Locate every Plasmodium vivax-infected red blood cell.
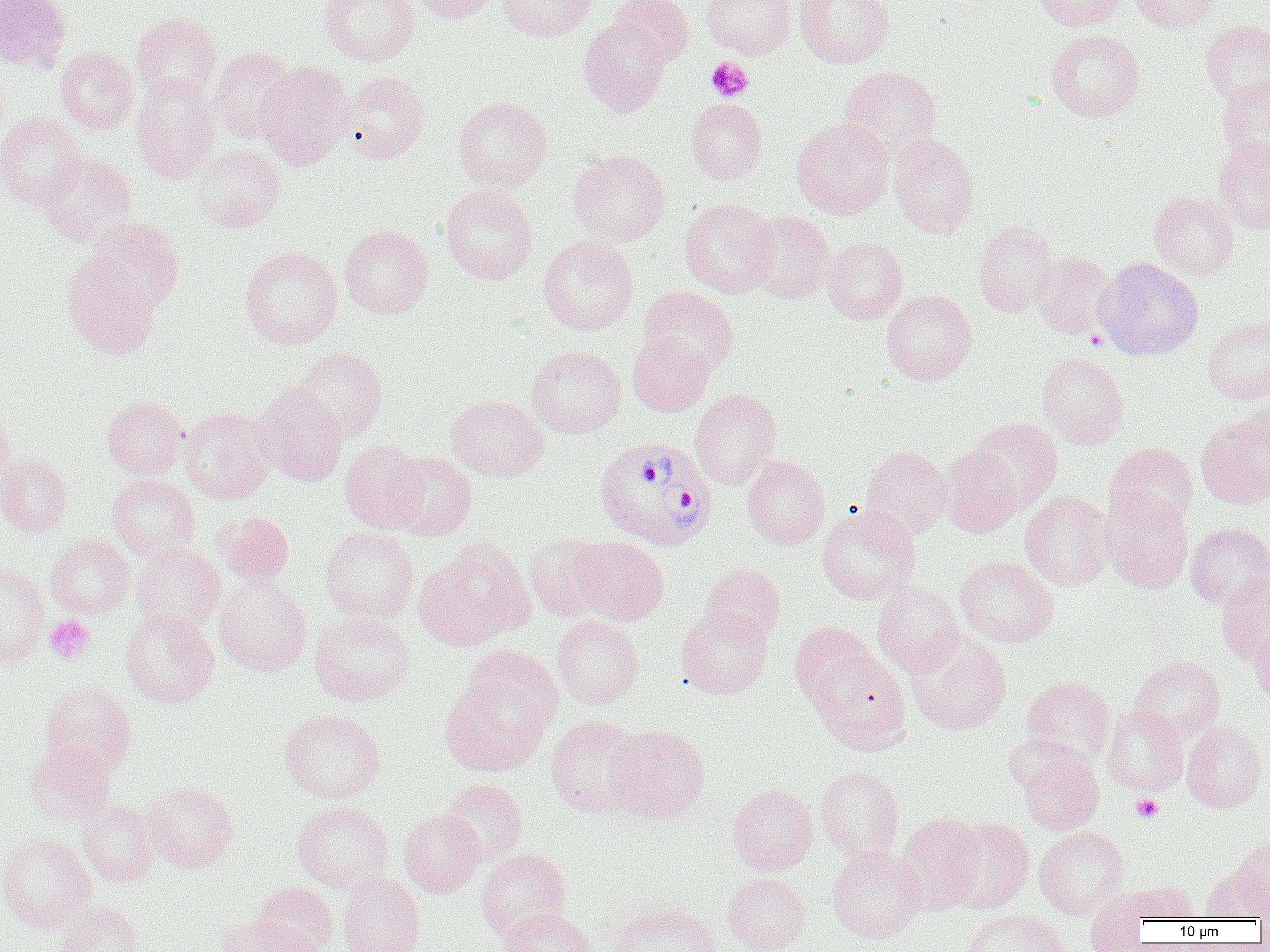
Approximate bounding boxes as named x1/y1/x2/y2 corners in pixels.
Plasmodium vivax-infected red blood cells: (x1=593, y1=436, x2=718, y2=552).

Summary:
  - Uninfected red blood cell locations: (x1=0, y1=0, x2=70, y2=73), (x1=320, y1=0, x2=419, y2=66), (x1=411, y1=0, x2=501, y2=23), (x1=497, y1=0, x2=596, y2=41), (x1=611, y1=0, x2=694, y2=66), (x1=702, y1=0, x2=795, y2=58), (x1=794, y1=0, x2=895, y2=68), (x1=1031, y1=0, x2=1128, y2=31), (x1=1130, y1=0, x2=1219, y2=33), (x1=131, y1=13, x2=222, y2=103), (x1=579, y1=17, x2=670, y2=116), (x1=1201, y1=20, x2=1270, y2=107), (x1=1046, y1=29, x2=1144, y2=121), (x1=55, y1=46, x2=137, y2=133), (x1=210, y1=47, x2=298, y2=142), (x1=254, y1=60, x2=353, y2=169), (x1=839, y1=65, x2=941, y2=157), (x1=340, y1=72, x2=430, y2=164), (x1=132, y1=75, x2=221, y2=183), (x1=1216, y1=76, x2=1270, y2=163), (x1=453, y1=96, x2=552, y2=191), (x1=686, y1=98, x2=767, y2=183), (x1=0, y1=113, x2=86, y2=209), (x1=791, y1=118, x2=894, y2=219), (x1=889, y1=132, x2=979, y2=237), (x1=1214, y1=136, x2=1270, y2=233), (x1=191, y1=144, x2=286, y2=232), (x1=568, y1=149, x2=671, y2=245), (x1=37, y1=152, x2=137, y2=245), (x1=440, y1=185, x2=538, y2=284), (x1=1149, y1=191, x2=1239, y2=280), (x1=679, y1=198, x2=779, y2=297), (x1=746, y1=211, x2=834, y2=304), (x1=87, y1=217, x2=185, y2=311), (x1=973, y1=220, x2=1058, y2=316), (x1=339, y1=225, x2=434, y2=318), (x1=538, y1=235, x2=638, y2=334), (x1=822, y1=235, x2=908, y2=324), (x1=240, y1=246, x2=343, y2=349), (x1=1031, y1=251, x2=1116, y2=338), (x1=63, y1=254, x2=160, y2=359), (x1=1094, y1=257, x2=1204, y2=360), (x1=639, y1=286, x2=739, y2=376), (x1=881, y1=290, x2=978, y2=385), (x1=1203, y1=316, x2=1270, y2=404), (x1=627, y1=331, x2=713, y2=415), (x1=526, y1=345, x2=626, y2=438), (x1=291, y1=347, x2=388, y2=442), (x1=1037, y1=352, x2=1129, y2=447), (x1=253, y1=381, x2=348, y2=486), (x1=690, y1=388, x2=782, y2=490), (x1=447, y1=395, x2=548, y2=480), (x1=101, y1=396, x2=186, y2=478), (x1=1237, y1=400, x2=1270, y2=482), (x1=180, y1=407, x2=276, y2=503), (x1=0, y1=410, x2=16, y2=496), (x1=1195, y1=413, x2=1270, y2=509), (x1=969, y1=417, x2=1062, y2=512), (x1=339, y1=440, x2=429, y2=533), (x1=1105, y1=442, x2=1198, y2=530), (x1=860, y1=445, x2=953, y2=539), (x1=940, y1=445, x2=1024, y2=537), (x1=389, y1=452, x2=477, y2=541), (x1=0, y1=455, x2=72, y2=536), (x1=742, y1=455, x2=829, y2=550), (x1=107, y1=475, x2=200, y2=559), (x1=1020, y1=490, x2=1113, y2=590), (x1=1100, y1=490, x2=1193, y2=593), (x1=817, y1=504, x2=919, y2=605), (x1=218, y1=511, x2=294, y2=587), (x1=1185, y1=522, x2=1270, y2=609), (x1=320, y1=527, x2=419, y2=623), (x1=524, y1=534, x2=610, y2=622), (x1=45, y1=535, x2=134, y2=617), (x1=569, y1=537, x2=669, y2=625), (x1=415, y1=541, x2=534, y2=649), (x1=131, y1=544, x2=225, y2=632), (x1=954, y1=555, x2=1059, y2=647), (x1=0, y1=562, x2=49, y2=667), (x1=701, y1=562, x2=786, y2=644), (x1=1215, y1=574, x2=1270, y2=665), (x1=214, y1=577, x2=312, y2=676), (x1=871, y1=580, x2=964, y2=676), (x1=675, y1=605, x2=773, y2=699), (x1=120, y1=608, x2=219, y2=707), (x1=309, y1=612, x2=415, y2=705), (x1=552, y1=615, x2=644, y2=708), (x1=1249, y1=621, x2=1270, y2=707), (x1=790, y1=622, x2=878, y2=712), (x1=907, y1=632, x2=1011, y2=735), (x1=811, y1=650, x2=910, y2=748), (x1=1129, y1=656, x2=1226, y2=740), (x1=441, y1=670, x2=553, y2=776), (x1=1021, y1=675, x2=1115, y2=763), (x1=42, y1=682, x2=137, y2=774), (x1=1102, y1=705, x2=1188, y2=795), (x1=279, y1=709, x2=385, y2=802), (x1=546, y1=715, x2=645, y2=817), (x1=1181, y1=721, x2=1267, y2=811), (x1=604, y1=724, x2=710, y2=823), (x1=25, y1=740, x2=116, y2=823), (x1=1018, y1=749, x2=1104, y2=834), (x1=816, y1=765, x2=904, y2=861), (x1=441, y1=778, x2=528, y2=865), (x1=143, y1=781, x2=238, y2=872), (x1=728, y1=783, x2=818, y2=874), (x1=77, y1=799, x2=159, y2=886), (x1=292, y1=801, x2=394, y2=892), (x1=399, y1=808, x2=485, y2=897), (x1=895, y1=812, x2=986, y2=913), (x1=944, y1=817, x2=1034, y2=913), (x1=1034, y1=826, x2=1129, y2=919), (x1=0, y1=833, x2=95, y2=930), (x1=1233, y1=834, x2=1270, y2=915), (x1=827, y1=845, x2=927, y2=943), (x1=475, y1=848, x2=571, y2=940), (x1=1200, y1=865, x2=1269, y2=924), (x1=338, y1=872, x2=425, y2=952), (x1=723, y1=872, x2=811, y2=952), (x1=252, y1=881, x2=338, y2=952), (x1=1125, y1=881, x2=1199, y2=922), (x1=1083, y1=888, x2=1157, y2=952), (x1=56, y1=902, x2=145, y2=952), (x1=609, y1=903, x2=722, y2=952), (x1=498, y1=906, x2=597, y2=952), (x1=961, y1=908, x2=1071, y2=952), (x1=218, y1=914, x2=318, y2=952)
  - Platelet locations: (x1=706, y1=57, x2=754, y2=101), (x1=1086, y1=329, x2=1107, y2=350), (x1=44, y1=615, x2=96, y2=664), (x1=1131, y1=793, x2=1163, y2=822)
  - Slide-level diagnosis: Plasmodium vivax
  - Image size: 1270×952 pixels
  - Modality: light microscopy
  - Magnification: 1000x
  - Preparation: thin blood smear
  - Field of view: one of a larger specimen